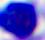
Photomicrograph. 400x magnification. A white blood cell is seen.